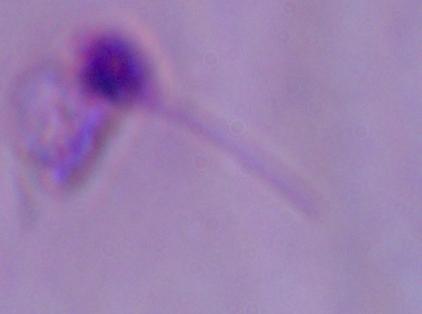

Summary:
  - Magnification: 1000x
  - Modality: photomicrograph
  - Identification: Leishmania